Give the extent of all Plasmodium ovale-infected red blood cells.
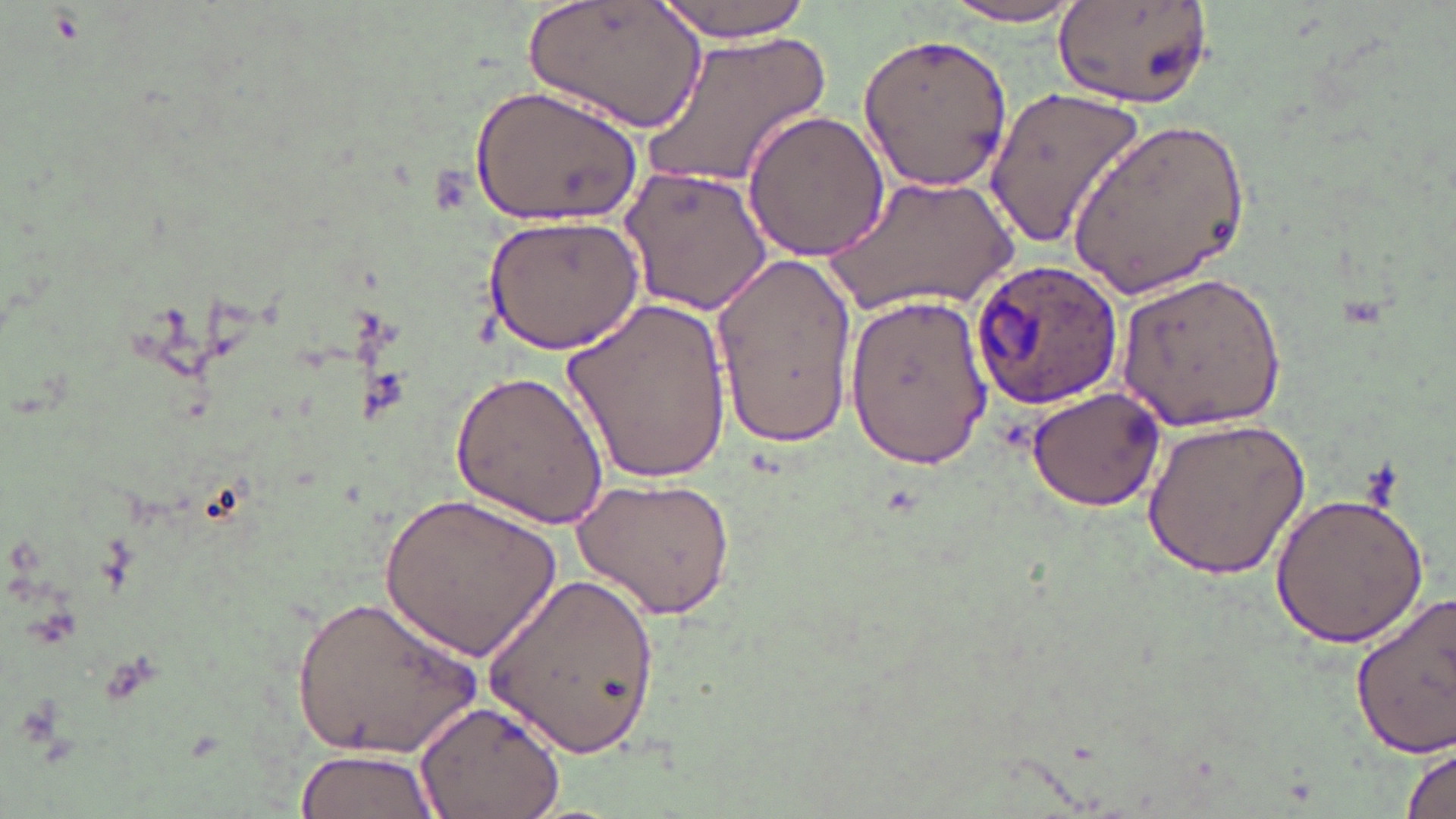

Approximate bounding boxes as [x1, y1, x2, y2] in pixels.
Plasmodium ovale-infected red blood cells: [966, 260, 1124, 414].

Uninfected red blood cell locations: [652, 0, 817, 41], [936, 2, 1090, 28], [528, 3, 701, 131], [1053, 3, 1215, 110], [645, 27, 831, 192], [855, 30, 1015, 194], [469, 84, 644, 226], [983, 86, 1145, 250], [742, 107, 888, 262], [1068, 115, 1253, 296], [621, 165, 773, 316], [825, 176, 1021, 315], [483, 213, 645, 353], [712, 250, 856, 449], [1114, 270, 1287, 432], [842, 293, 993, 466], [563, 296, 734, 487], [448, 367, 608, 529], [1025, 385, 1169, 512], [1141, 417, 1311, 580], [573, 474, 740, 619], [1268, 488, 1429, 649], [381, 491, 561, 664], [488, 566, 664, 759], [290, 590, 480, 762], [1349, 592, 1456, 763], [415, 697, 568, 819], [1400, 740, 1455, 819], [293, 748, 441, 819]. Slide-level diagnosis: Plasmodium ovale. Image is 1456×819 pixels. Captured at 1000x magnification. May-Grünwald-Giemsa stain. Single field of view. Light microscopy. Thin blood film.